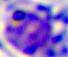

Summary:
  - Modality: micrograph
  - Identification: leukocyte
  - Magnification: 400x